Outline each blood parasite and name the species.
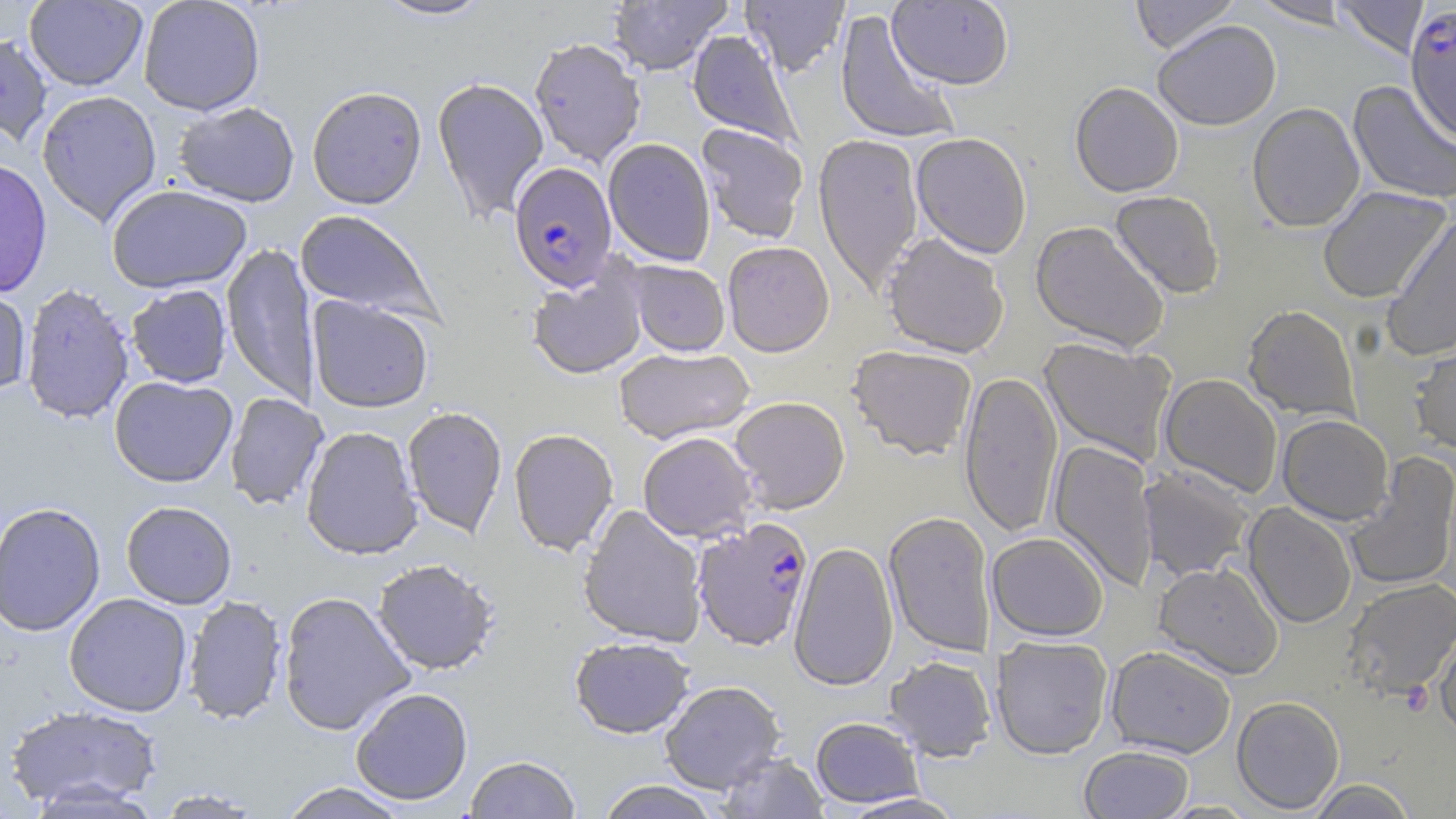
Approximate bounding boxes as (x1,y1)-(x2,y2) corner pairs in pixels.
Plasmodium falciparum-infected red blood cells: (1405,4)-(1456,143), (509,161)-(618,292), (693,517)-(814,651).
No Plasmodium ovale, Plasmodium malariae, Plasmodium vivax, Babesia divergens, or Trypanosoma brucei observed.

Summary:
  - Uninfected red blood cell locations: (24,0)-(148,92), (138,0)-(265,116), (374,0)-(494,21), (607,0)-(731,76), (740,0)-(851,78), (887,0)-(1014,89), (1130,0)-(1241,54), (1248,0)-(1357,28), (1331,0)-(1429,60), (834,9)-(961,147), (1152,20)-(1281,131), (687,29)-(802,148), (0,32)-(53,147), (529,37)-(646,167), (432,76)-(549,224), (1348,81)-(1456,205), (1070,82)-(1184,198), (306,85)-(427,210), (36,90)-(162,226), (173,101)-(300,207), (1247,102)-(1365,233), (696,123)-(809,243), (813,133)-(924,294), (911,133)-(1032,260), (603,138)-(715,267), (0,157)-(53,298), (106,184)-(252,294), (1317,186)-(1452,304), (1109,190)-(1225,299), (294,209)-(443,324), (1382,216)-(1456,364), (1030,221)-(1171,353), (882,233)-(1009,359), (722,241)-(835,357), (221,242)-(319,406), (625,260)-(730,357), (527,265)-(648,381), (21,283)-(135,424), (126,284)-(232,388), (0,286)-(32,398), (307,296)-(434,413), (1242,305)-(1361,422), (1410,336)-(1456,456), (1039,337)-(1176,466), (614,346)-(755,445), (847,346)-(977,461), (959,370)-(1063,539), (1159,373)-(1282,498), (109,375)-(238,488), (224,392)-(328,511), (729,396)-(850,515), (402,406)-(507,539), (1277,414)-(1393,525), (301,425)-(423,560), (508,428)-(619,557), (638,432)-(758,543), (1048,439)-(1159,592), (1344,453)-(1456,593), (1138,465)-(1255,582), (120,501)-(237,609), (0,502)-(106,636), (1243,503)-(1357,628), (578,504)-(707,647), (883,512)-(996,658), (986,532)-(1109,642), (788,541)-(899,692), (372,559)-(499,676), (1153,561)-(1284,680), (1342,577)-(1456,699), (277,591)-(415,736), (64,593)-(192,716), (182,595)-(288,726), (1435,617)-(1456,741), (570,636)-(695,739), (992,636)-(1113,759), (1105,645)-(1237,758), (884,655)-(996,761), (659,680)-(785,793), (351,687)-(473,806), (1232,696)-(1345,814), (5,704)-(163,811), (810,717)-(924,808), (1079,745)-(1194,818), (717,752)-(829,818), (464,756)-(581,819), (1306,778)-(1419,818), (596,780)-(722,819), (277,782)-(411,819), (150,788)-(268,817), (836,793)-(970,818), (1156,800)-(1259,818)
  - Slide-level diagnosis: Plasmodium falciparum
  - Image size: 1456×819 pixels
  - Preparation: thin blood film
  - Magnification: 1000x
  - Stain: May-Grünwald-Giemsa
  - Modality: light microscopy
  - Field of view: single